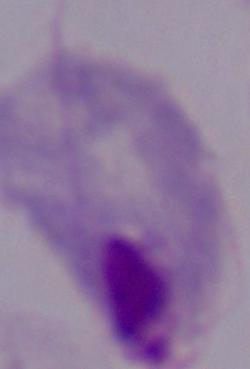

magnification = 1000x
modality = photomicrograph
identification = trichomonad